Point out each leukocyte.
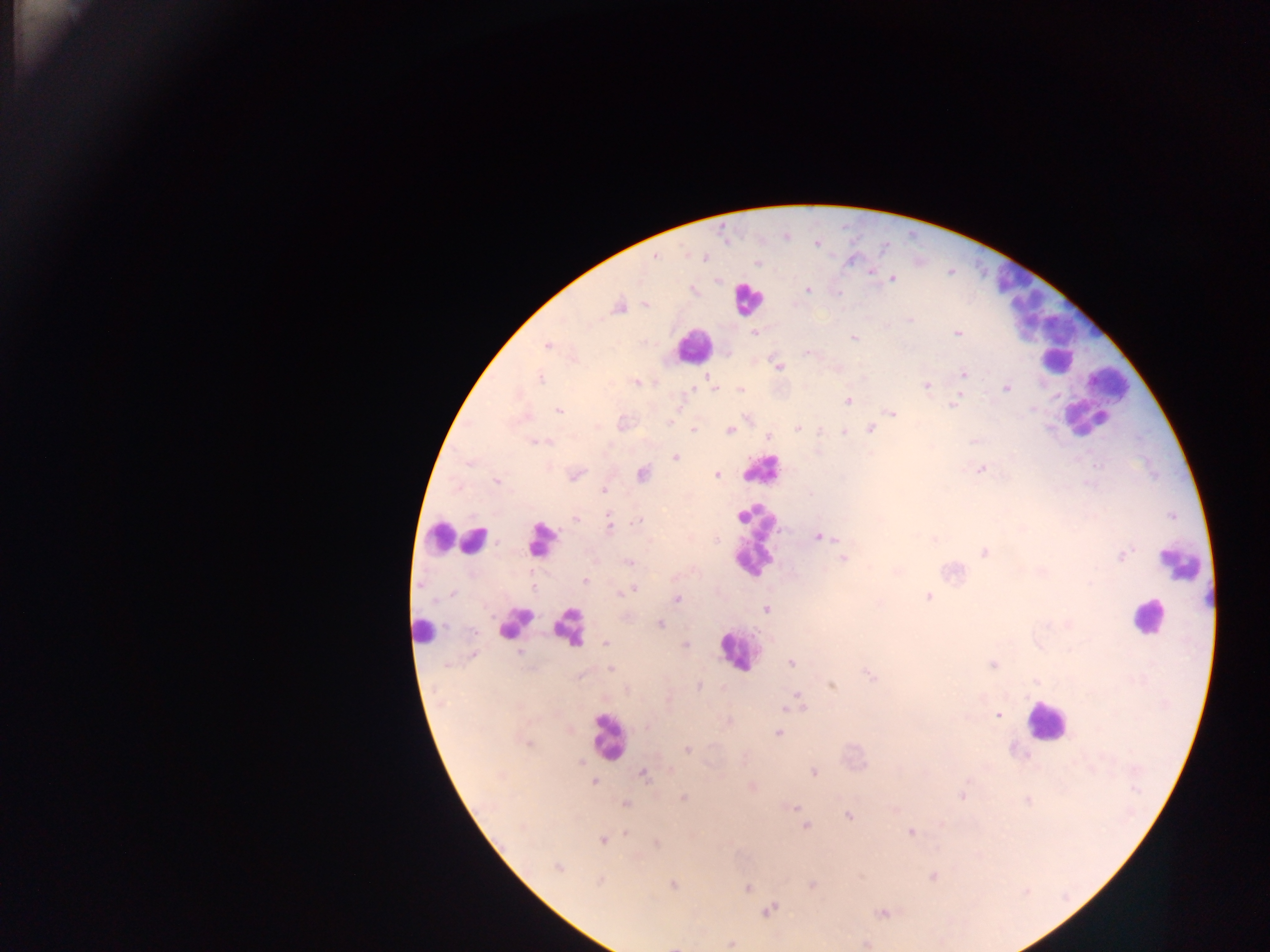

Approximate centers as (x, y) in pixels.
Leukocytes: (1009, 279), (747, 298), (1088, 313), (1022, 316), (1047, 327), (693, 346), (1058, 362), (1109, 381), (1096, 400), (1084, 418), (761, 469), (440, 536), (473, 540), (755, 540), (540, 541), (1181, 565), (1204, 598), (1148, 617), (514, 623), (568, 627), (423, 631), (737, 651), (1045, 722), (608, 736).

Summary:
  - Plasmodium parasite locations: (816, 242), (654, 256), (703, 258), (757, 262), (871, 272), (716, 279), (892, 279), (807, 289), (693, 290), (645, 305), (619, 306), (756, 333), (957, 333), (853, 337), (548, 345), (573, 359), (778, 367), (963, 375), (539, 378), (710, 379), (636, 382), (925, 385), (713, 387), (1006, 388), (740, 391), (847, 400), (953, 405), (559, 410), (891, 414), (798, 428), (870, 429), (694, 430), (820, 430), (729, 431), (845, 433), (767, 437), (538, 441), (675, 457), (981, 469), (574, 474), (641, 474), (717, 474), (497, 480), (604, 489), (609, 516), (575, 518), (634, 521), (609, 526), (819, 536), (933, 538), (984, 552), (1120, 556), (843, 559), (629, 562), (896, 570), (584, 580), (632, 590), (927, 596), (676, 599), (765, 608), (660, 624), (605, 643), (685, 645), (473, 655), (790, 662), (993, 665), (611, 668), (870, 675), (698, 686), (831, 686), (797, 698), (791, 706), (802, 708), (997, 715), (728, 721), (778, 732), (686, 749), (812, 772), (642, 774), (593, 782), (751, 787), (963, 796), (683, 797), (625, 803), (793, 806), (893, 808), (849, 816), (805, 826), (910, 832), (603, 839), (656, 843), (557, 867), (933, 876), (599, 881), (672, 884), (812, 884), (748, 887), (768, 909), (882, 913), (731, 943), (866, 943), (677, 945)
  - Field of view: single
  - Preparation: thick blood film
  - Country: Ghana
  - Image size: 1270×952 pixels
  - Capture: mobile-phone photograph through a microscope